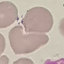

Summary:
  - Malaria status: uninfected
  - Capture: smartphone through the microscope eyepiece
  - Preparation: thin blood film
  - Stain: Giemsa
  - Image type: cell patch, automatically extracted from a larger field of view and resized to 64 × 64 pixels